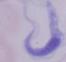
magnification = 1000x
identification = trypanosome
modality = photomicrograph